Name the parasite shown.
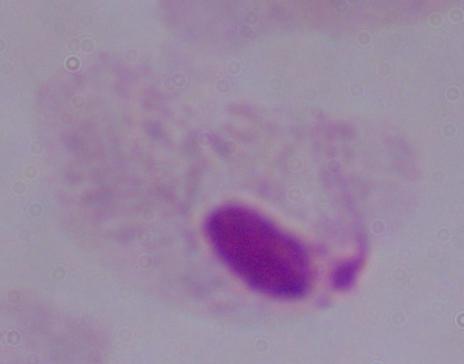

A trichomonad.

Photomicrograph. 1000x magnification.